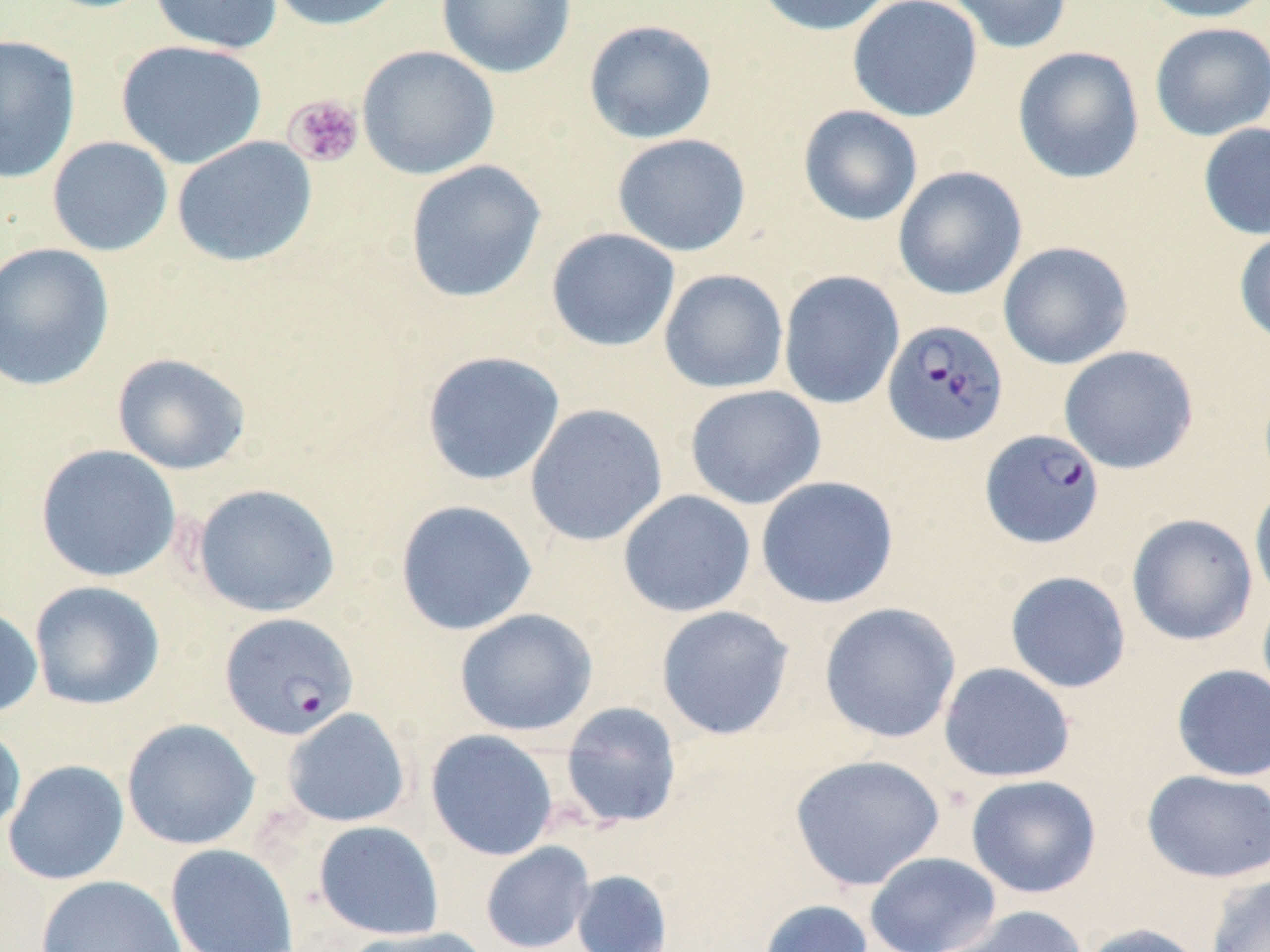
Approximate bounding boxes as named x1/y1/x2/y2 corners in pixels. Plasmodium falciparum-infected red blood cell locations: (x1=882, y1=318, x2=1009, y2=446), (x1=980, y1=428, x2=1105, y2=549), (x1=220, y1=612, x2=358, y2=740). Uninfected red blood cell locations: (x1=149, y1=0, x2=283, y2=54), (x1=264, y1=0, x2=409, y2=31), (x1=436, y1=0, x2=577, y2=79), (x1=752, y1=0, x2=897, y2=36), (x1=847, y1=0, x2=983, y2=122), (x1=943, y1=0, x2=1073, y2=54), (x1=1140, y1=0, x2=1270, y2=23), (x1=583, y1=19, x2=718, y2=144), (x1=1149, y1=22, x2=1270, y2=141), (x1=0, y1=34, x2=81, y2=184), (x1=115, y1=39, x2=268, y2=169), (x1=356, y1=45, x2=500, y2=180), (x1=1012, y1=46, x2=1145, y2=184), (x1=798, y1=105, x2=923, y2=226), (x1=1198, y1=122, x2=1270, y2=240), (x1=612, y1=133, x2=752, y2=257), (x1=47, y1=136, x2=173, y2=257), (x1=171, y1=136, x2=317, y2=267), (x1=404, y1=160, x2=546, y2=303), (x1=892, y1=166, x2=1027, y2=300), (x1=1233, y1=226, x2=1270, y2=347), (x1=546, y1=227, x2=680, y2=352), (x1=998, y1=240, x2=1134, y2=370), (x1=0, y1=242, x2=116, y2=392), (x1=658, y1=268, x2=789, y2=394), (x1=778, y1=270, x2=905, y2=409), (x1=1058, y1=345, x2=1199, y2=474), (x1=420, y1=350, x2=565, y2=486), (x1=111, y1=352, x2=252, y2=475), (x1=684, y1=385, x2=827, y2=510), (x1=525, y1=403, x2=668, y2=546), (x1=35, y1=444, x2=181, y2=583), (x1=756, y1=475, x2=899, y2=609), (x1=1249, y1=481, x2=1270, y2=607), (x1=190, y1=483, x2=341, y2=618), (x1=618, y1=489, x2=756, y2=618), (x1=394, y1=499, x2=538, y2=636), (x1=1126, y1=513, x2=1258, y2=646), (x1=1004, y1=570, x2=1131, y2=694), (x1=29, y1=581, x2=165, y2=710), (x1=1256, y1=590, x2=1270, y2=711), (x1=819, y1=602, x2=961, y2=744), (x1=0, y1=605, x2=43, y2=719), (x1=655, y1=605, x2=794, y2=740), (x1=455, y1=608, x2=599, y2=737), (x1=938, y1=662, x2=1075, y2=783), (x1=1171, y1=664, x2=1270, y2=782), (x1=559, y1=701, x2=683, y2=830), (x1=281, y1=707, x2=411, y2=828), (x1=121, y1=718, x2=261, y2=850), (x1=0, y1=724, x2=27, y2=839), (x1=425, y1=729, x2=559, y2=861), (x1=788, y1=753, x2=946, y2=891), (x1=2, y1=759, x2=130, y2=885), (x1=1141, y1=769, x2=1270, y2=883), (x1=965, y1=774, x2=1102, y2=898), (x1=313, y1=820, x2=445, y2=939), (x1=480, y1=841, x2=595, y2=952), (x1=165, y1=844, x2=299, y2=952), (x1=864, y1=851, x2=1002, y2=952), (x1=571, y1=869, x2=673, y2=952), (x1=1204, y1=873, x2=1270, y2=952), (x1=36, y1=874, x2=188, y2=952), (x1=757, y1=899, x2=874, y2=952), (x1=939, y1=905, x2=1089, y2=952), (x1=1078, y1=922, x2=1209, y2=952), (x1=341, y1=926, x2=493, y2=952). Platelet locations: (x1=284, y1=95, x2=364, y2=168). Slide-level diagnosis: Plasmodium falciparum. Image is 1270×952 pixels. 1000x magnification. Thin blood smear. One field of a larger specimen. May-Grünwald-Giemsa stain. Light microscopy.